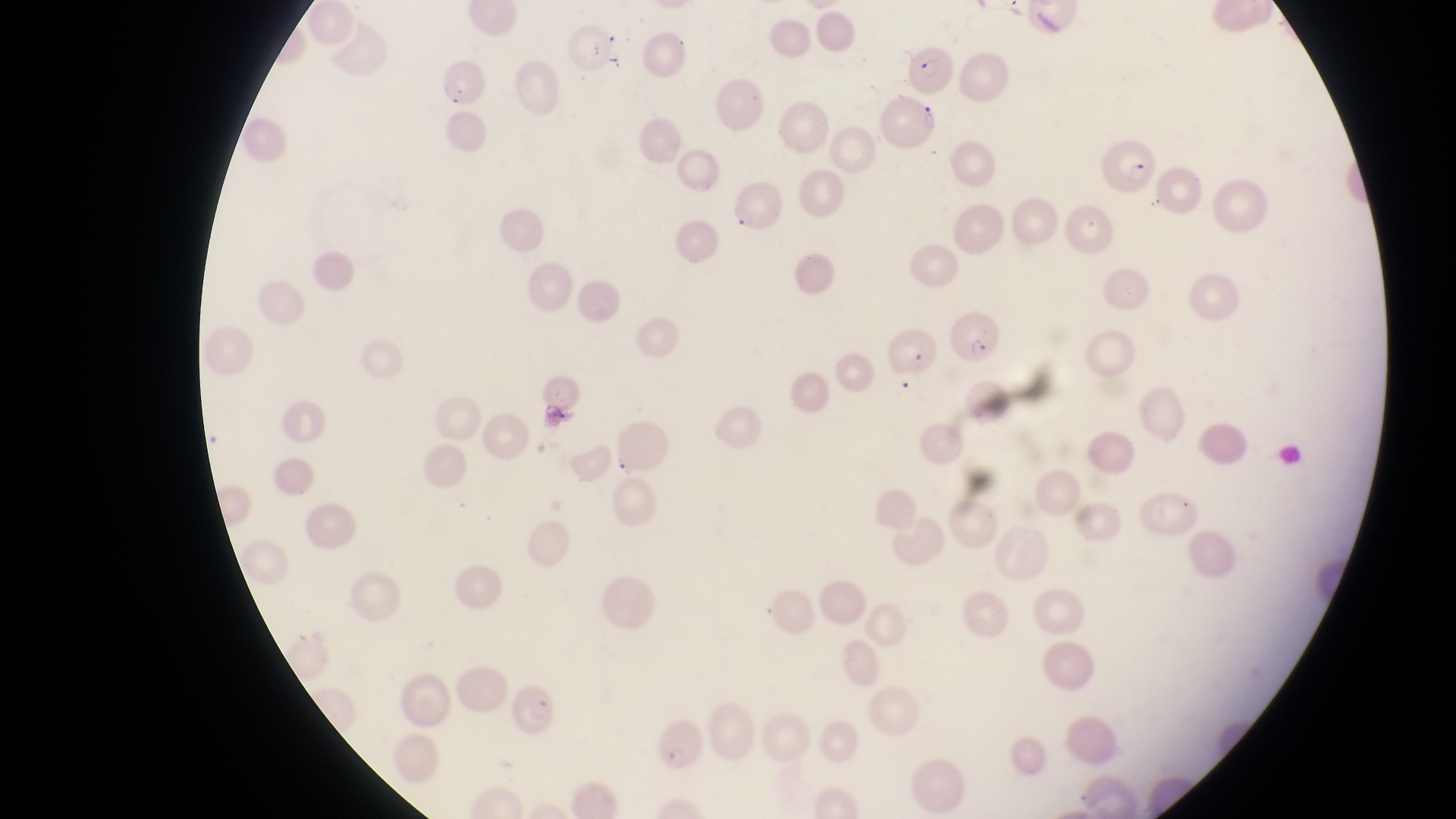
Approximate bounding boxes as left top right bottom in pixels. Parasitised red blood cell locations: 901 39 954 95; 439 63 485 109; 880 92 936 148; 1105 133 1161 199; 949 310 1004 362; 883 328 936 375; 510 684 560 739; 655 710 704 773. Captured by a smartphone held over the eyepiece of an Olympus CX-23 microscope. Collected in Uganda. Thin blood film. One field of view. Image is 1456×819 pixels. At a magnification of 1000x.